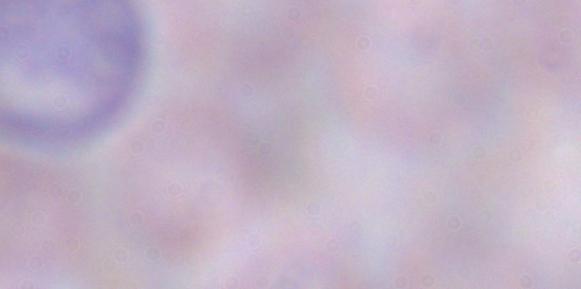
magnification = 1000x
identification = trypanosome
modality = micrograph